Assess this cell for malaria.
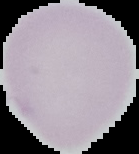
Uninfected.

image type = segmented cell region with the area outside set to black
image size = 139×154 pixels
preparation = thin blood film